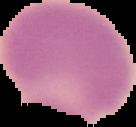
result: negative for malaria parasites
preparation: thin blood film
image_size: 136×127 pixels
image_type: segmented cell region with the area outside set to black